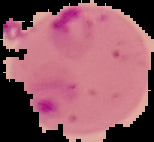
Summary:
  - Preparation: thin blood film
  - Result: Plasmodium parasites detected
  - Image type: segmented cell region on a black background
  - Image size: 154×142 pixels